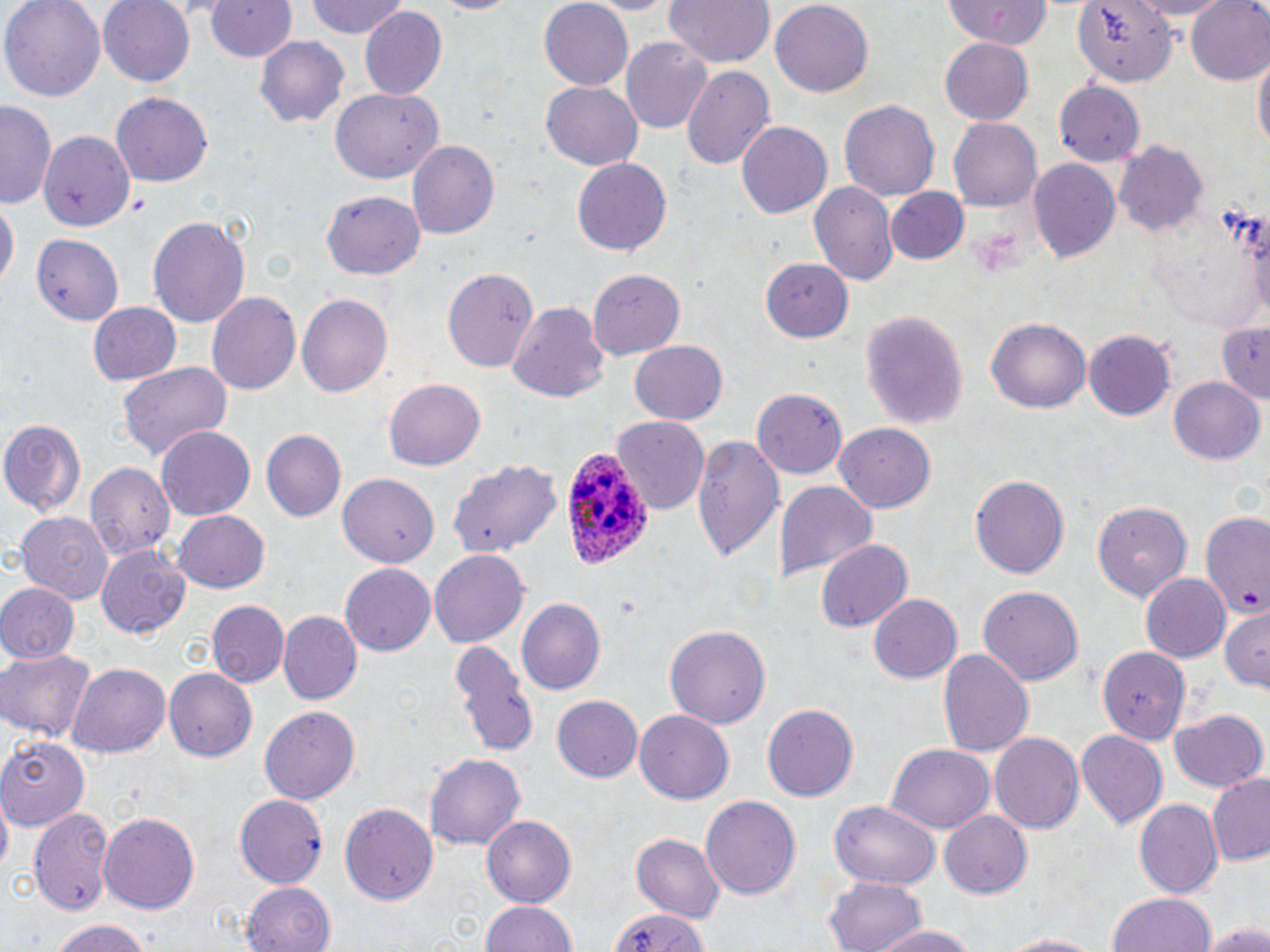

Approximate bounding boxes as [x1, y1, x2, y2] in pixels. Uninfected red blood cell locations: [2, 0, 106, 99], [100, 0, 196, 85], [200, 0, 299, 63], [305, 0, 412, 41], [577, 0, 681, 14], [663, 0, 778, 68], [769, 0, 872, 94], [951, 0, 1051, 52], [1069, 0, 1181, 86], [1123, 0, 1238, 19], [1184, 0, 1270, 86], [538, 2, 634, 89], [359, 8, 447, 101], [253, 36, 349, 126], [620, 37, 713, 134], [941, 40, 1034, 123], [1253, 54, 1268, 158], [680, 64, 777, 173], [540, 80, 644, 171], [1054, 80, 1144, 167], [331, 87, 443, 183], [110, 93, 214, 187], [839, 98, 943, 201], [0, 103, 56, 210], [948, 117, 1042, 210], [736, 122, 833, 221], [38, 130, 134, 231], [407, 140, 498, 240], [1114, 142, 1209, 235], [572, 157, 673, 256], [1027, 157, 1119, 263], [808, 181, 897, 288], [885, 187, 970, 266], [322, 191, 425, 278], [1, 200, 17, 296], [148, 214, 249, 326], [31, 233, 124, 326], [758, 257, 851, 341], [442, 267, 537, 371], [586, 269, 686, 360], [206, 292, 304, 396], [296, 293, 392, 398], [87, 301, 181, 386], [507, 302, 609, 404], [858, 308, 967, 430], [987, 314, 1090, 411], [1212, 320, 1270, 401], [1084, 329, 1177, 419], [630, 341, 727, 426], [118, 361, 234, 461], [1168, 377, 1264, 467], [385, 379, 485, 472], [751, 387, 848, 479], [611, 416, 709, 514], [1, 418, 86, 516], [832, 423, 935, 513], [155, 426, 257, 521], [262, 429, 346, 521], [691, 431, 783, 565], [449, 457, 564, 560], [82, 462, 175, 564], [336, 473, 438, 567], [969, 474, 1071, 579], [775, 479, 877, 585], [1090, 499, 1192, 602], [172, 510, 271, 593], [16, 511, 114, 603], [1199, 511, 1270, 621], [817, 538, 912, 630], [97, 545, 192, 638], [429, 549, 529, 648], [340, 562, 436, 655], [1138, 574, 1229, 664], [0, 582, 78, 661], [978, 586, 1083, 686], [869, 594, 962, 683], [516, 598, 607, 697], [206, 600, 289, 689], [1221, 610, 1270, 687], [279, 612, 361, 705], [665, 624, 770, 731], [452, 641, 536, 756], [937, 646, 1036, 758], [0, 648, 96, 742], [1098, 648, 1186, 745], [69, 663, 170, 760], [165, 669, 258, 762], [552, 695, 642, 783], [764, 702, 860, 803], [259, 705, 361, 805], [1170, 707, 1269, 792], [635, 710, 735, 803], [1075, 728, 1165, 826], [989, 730, 1085, 834], [0, 737, 89, 830], [885, 744, 995, 832], [425, 751, 528, 851], [1208, 774, 1270, 865], [700, 794, 801, 901], [233, 795, 327, 889], [1135, 798, 1222, 897], [341, 799, 438, 905], [828, 801, 940, 888], [27, 806, 115, 917], [939, 809, 1032, 899], [100, 812, 200, 912], [483, 816, 576, 904], [630, 832, 724, 922], [826, 873, 928, 952], [240, 879, 336, 950], [1107, 890, 1215, 952], [480, 898, 577, 952], [607, 905, 716, 952], [46, 918, 155, 952], [871, 920, 982, 952], [1200, 921, 1270, 952], [991, 931, 1113, 951]. Plasmodium ovale-infected red blood cell locations: [563, 448, 656, 569]. Slide-level diagnosis: Plasmodium ovale. Thin blood smear. May-Grünwald-Giemsa stain. Light microscopy. Image is 1270×952 pixels. Single field of view. Captured at 1000x magnification.